Assess the morphology of the erythrocytes.
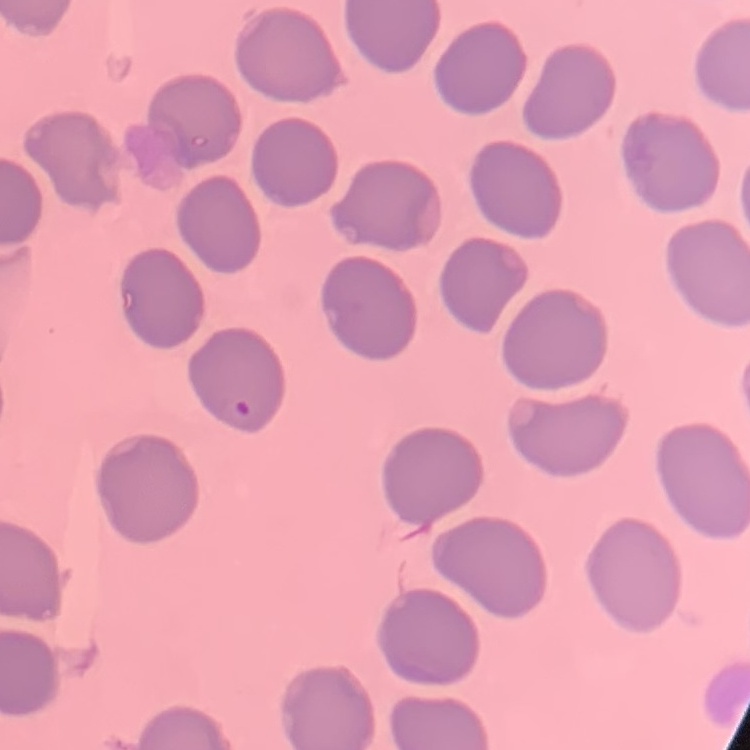
No rouleaux formation.

Field's or Giemsa stain. One tile cut from a larger photomicrograph. Thin peripheral smear.